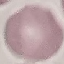

Summary:
  - Malaria status: uninfected
  - Preparation: thin blood smear
  - Image type: cell patch, automatically extracted from a larger field of view and resized to 64 × 64 pixels
  - Capture: smartphone camera at the microscope eyepiece
  - Stain: Giemsa